Describe the morphology of the erythrocytes.
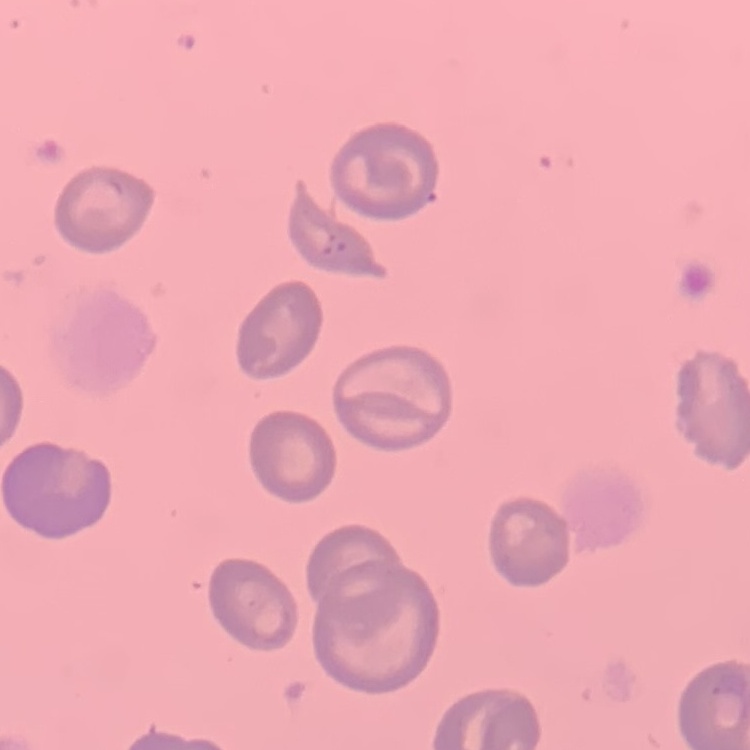

They show no rouleaux formation.

Thin blood smear. Field's or Giemsa stain. One tile cut from a larger photomicrograph.